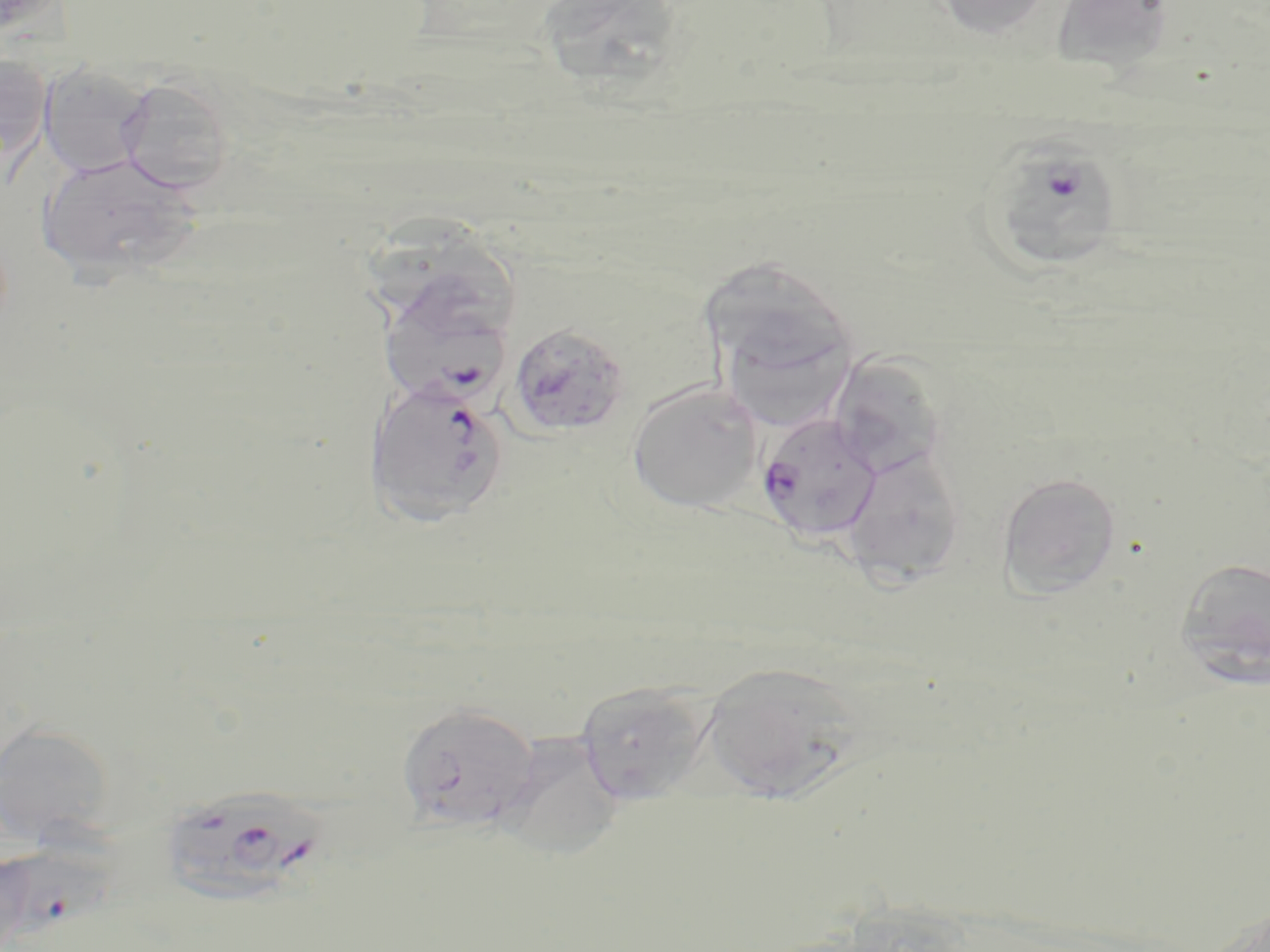
Summary:
  - Coordinate format: approximate bounding boxes as named x1/y1/x2/y2 corners in pixels
  - Plasmodium falciparum-infected red blood cell locations: (x1=980, y1=141, x2=1128, y2=271), (x1=377, y1=285, x2=515, y2=412), (x1=363, y1=377, x2=510, y2=528), (x1=757, y1=411, x2=883, y2=542), (x1=169, y1=792, x2=337, y2=902), (x1=0, y1=847, x2=125, y2=951)
  - Uninfected red blood cell locations: (x1=547, y1=0, x2=685, y2=93), (x1=930, y1=0, x2=1053, y2=38), (x1=1050, y1=0, x2=1174, y2=69), (x1=0, y1=52, x2=51, y2=172), (x1=38, y1=60, x2=154, y2=179), (x1=115, y1=75, x2=236, y2=194), (x1=35, y1=151, x2=203, y2=281), (x1=366, y1=214, x2=517, y2=333), (x1=696, y1=255, x2=859, y2=388), (x1=723, y1=314, x2=845, y2=426), (x1=508, y1=322, x2=630, y2=438), (x1=843, y1=356, x2=951, y2=486), (x1=626, y1=381, x2=764, y2=514), (x1=841, y1=447, x2=967, y2=585), (x1=996, y1=471, x2=1122, y2=599), (x1=1175, y1=556, x2=1270, y2=690), (x1=700, y1=661, x2=865, y2=800), (x1=572, y1=680, x2=717, y2=805), (x1=396, y1=700, x2=540, y2=834), (x1=0, y1=720, x2=116, y2=848), (x1=503, y1=725, x2=625, y2=863)
  - Slide-level diagnosis: Plasmodium falciparum
  - Image size: 1270×952 pixels
  - Magnification: 1000x
  - Modality: light microscopy
  - Stain: May-Grünwald-Giemsa
  - Preparation: thin blood film
  - Field of view: one of a larger specimen